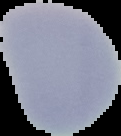
Summary:
  - Result: no malaria parasites detected
  - Image size: 121×136 pixels
  - Preparation: thin blood smear
  - Image type: segmented cell region on a black background